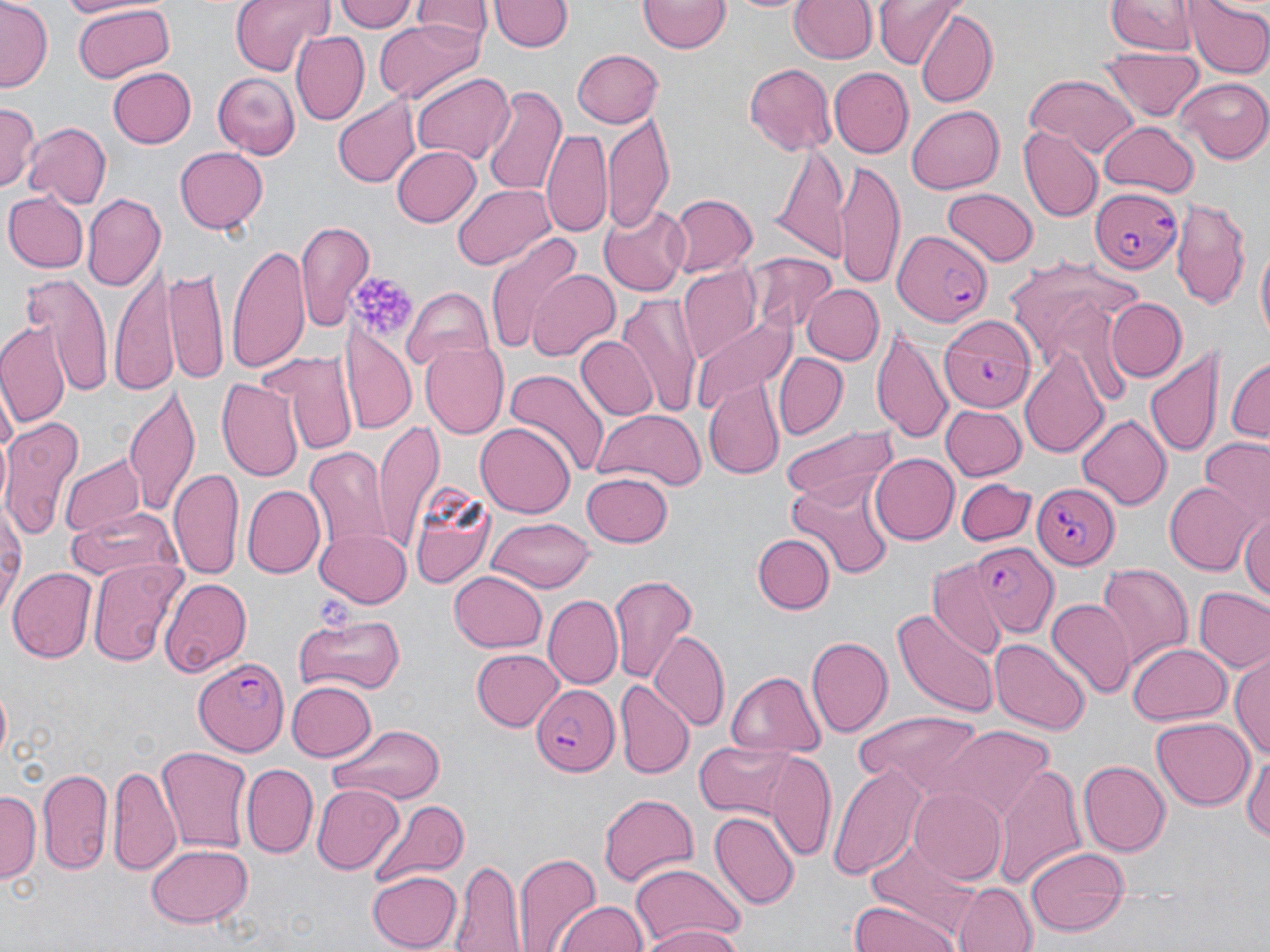
slide-level diagnosis = Plasmodium falciparum
modality = light microscopy
preparation = thin blood smear
stain = May-Grünwald-Giemsa
field of view = one of a larger specimen
image size = 1270×952 pixels
magnification = 1000x
platelet locations = approximate bounding boxes as named x1/y1/x2/y2 corners in pixels: (x1=350, y1=274, x2=417, y2=338)
uninfected red blood cell locations = approximate bounding boxes as named x1/y1/x2/y2 corners in pixels: (x1=1, y1=0, x2=51, y2=92), (x1=229, y1=0, x2=335, y2=75), (x1=333, y1=0, x2=416, y2=31), (x1=490, y1=0, x2=570, y2=54), (x1=722, y1=0, x2=814, y2=15), (x1=789, y1=0, x2=876, y2=64), (x1=872, y1=0, x2=963, y2=67), (x1=1105, y1=0, x2=1199, y2=56), (x1=410, y1=1, x2=490, y2=49), (x1=639, y1=1, x2=729, y2=54), (x1=1186, y1=1, x2=1269, y2=78), (x1=67, y1=3, x2=179, y2=82), (x1=913, y1=9, x2=997, y2=108), (x1=373, y1=20, x2=483, y2=103), (x1=291, y1=32, x2=368, y2=124), (x1=572, y1=47, x2=663, y2=128), (x1=1102, y1=48, x2=1203, y2=120), (x1=742, y1=62, x2=837, y2=155), (x1=105, y1=66, x2=196, y2=149), (x1=828, y1=69, x2=913, y2=158), (x1=411, y1=71, x2=512, y2=163), (x1=212, y1=72, x2=301, y2=159), (x1=1025, y1=73, x2=1140, y2=159), (x1=1177, y1=77, x2=1270, y2=163), (x1=479, y1=85, x2=565, y2=197), (x1=332, y1=95, x2=418, y2=189), (x1=0, y1=102, x2=39, y2=193), (x1=907, y1=103, x2=1003, y2=195), (x1=603, y1=110, x2=675, y2=233), (x1=24, y1=121, x2=113, y2=207), (x1=1098, y1=121, x2=1199, y2=198), (x1=1018, y1=125, x2=1100, y2=221), (x1=542, y1=130, x2=612, y2=241), (x1=768, y1=143, x2=851, y2=261), (x1=174, y1=145, x2=268, y2=236), (x1=391, y1=145, x2=480, y2=228), (x1=834, y1=162, x2=905, y2=287), (x1=452, y1=183, x2=554, y2=270), (x1=943, y1=188, x2=1040, y2=265), (x1=4, y1=191, x2=88, y2=272), (x1=82, y1=194, x2=165, y2=293), (x1=666, y1=194, x2=757, y2=278), (x1=1170, y1=199, x2=1251, y2=311), (x1=599, y1=204, x2=687, y2=298), (x1=295, y1=219, x2=372, y2=331), (x1=484, y1=232, x2=586, y2=354), (x1=225, y1=236, x2=312, y2=378), (x1=1253, y1=242, x2=1269, y2=354), (x1=749, y1=254, x2=836, y2=335), (x1=1002, y1=254, x2=1148, y2=387), (x1=109, y1=262, x2=177, y2=394), (x1=168, y1=263, x2=229, y2=390), (x1=678, y1=264, x2=760, y2=362), (x1=527, y1=268, x2=619, y2=360), (x1=21, y1=273, x2=113, y2=394), (x1=803, y1=283, x2=882, y2=365), (x1=403, y1=286, x2=494, y2=372), (x1=618, y1=292, x2=701, y2=419), (x1=1108, y1=298, x2=1185, y2=383), (x1=691, y1=311, x2=795, y2=418), (x1=342, y1=314, x2=416, y2=436), (x1=0, y1=317, x2=71, y2=433), (x1=873, y1=323, x2=955, y2=449), (x1=575, y1=336, x2=656, y2=421), (x1=421, y1=340, x2=509, y2=439), (x1=1145, y1=344, x2=1223, y2=465), (x1=1020, y1=348, x2=1110, y2=459), (x1=263, y1=350, x2=354, y2=455), (x1=774, y1=353, x2=847, y2=439), (x1=1226, y1=358, x2=1269, y2=446), (x1=503, y1=370, x2=609, y2=481), (x1=217, y1=374, x2=305, y2=482), (x1=704, y1=380, x2=782, y2=477), (x1=121, y1=383, x2=201, y2=518), (x1=939, y1=402, x2=1026, y2=481), (x1=591, y1=405, x2=706, y2=491), (x1=1075, y1=414, x2=1172, y2=509), (x1=4, y1=417, x2=83, y2=539), (x1=372, y1=417, x2=442, y2=551), (x1=476, y1=422, x2=574, y2=518), (x1=781, y1=424, x2=903, y2=508), (x1=1198, y1=441, x2=1270, y2=527), (x1=305, y1=445, x2=389, y2=553), (x1=868, y1=453, x2=958, y2=545), (x1=59, y1=454, x2=147, y2=541), (x1=170, y1=467, x2=245, y2=579), (x1=582, y1=473, x2=674, y2=548), (x1=786, y1=473, x2=894, y2=579), (x1=957, y1=477, x2=1035, y2=546), (x1=404, y1=480, x2=492, y2=592), (x1=1163, y1=481, x2=1258, y2=575), (x1=239, y1=484, x2=324, y2=579), (x1=0, y1=500, x2=25, y2=618), (x1=66, y1=507, x2=183, y2=587), (x1=1241, y1=508, x2=1270, y2=601), (x1=485, y1=517, x2=596, y2=591), (x1=314, y1=527, x2=411, y2=607), (x1=753, y1=534, x2=834, y2=614), (x1=87, y1=557, x2=184, y2=669), (x1=928, y1=560, x2=1010, y2=657), (x1=1094, y1=562, x2=1192, y2=670), (x1=10, y1=566, x2=96, y2=664), (x1=449, y1=570, x2=547, y2=652), (x1=607, y1=572, x2=698, y2=683), (x1=161, y1=577, x2=252, y2=680), (x1=1193, y1=587, x2=1270, y2=674), (x1=543, y1=595, x2=622, y2=687), (x1=1046, y1=598, x2=1134, y2=698), (x1=890, y1=606, x2=999, y2=719), (x1=291, y1=613, x2=408, y2=695), (x1=651, y1=631, x2=729, y2=730), (x1=805, y1=637, x2=892, y2=740), (x1=992, y1=638, x2=1088, y2=732), (x1=1128, y1=644, x2=1230, y2=728), (x1=471, y1=648, x2=563, y2=731), (x1=1232, y1=654, x2=1270, y2=765), (x1=725, y1=671, x2=825, y2=756), (x1=283, y1=680, x2=376, y2=764), (x1=614, y1=680, x2=693, y2=778), (x1=851, y1=709, x2=993, y2=799), (x1=1152, y1=715, x2=1254, y2=808), (x1=326, y1=722, x2=447, y2=806), (x1=935, y1=726, x2=1056, y2=824), (x1=692, y1=741, x2=806, y2=820), (x1=156, y1=744, x2=252, y2=856), (x1=1242, y1=747, x2=1270, y2=849), (x1=769, y1=751, x2=837, y2=862), (x1=1077, y1=760, x2=1168, y2=857), (x1=107, y1=762, x2=180, y2=873), (x1=829, y1=762, x2=926, y2=880), (x1=241, y1=763, x2=317, y2=857), (x1=993, y1=764, x2=1087, y2=889), (x1=38, y1=769, x2=113, y2=876), (x1=311, y1=784, x2=403, y2=874), (x1=909, y1=786, x2=1008, y2=885), (x1=2, y1=790, x2=38, y2=884), (x1=597, y1=793, x2=699, y2=891), (x1=369, y1=799, x2=469, y2=886), (x1=709, y1=810, x2=799, y2=910), (x1=145, y1=843, x2=254, y2=929), (x1=1026, y1=845, x2=1129, y2=936), (x1=513, y1=848, x2=603, y2=952), (x1=451, y1=859, x2=523, y2=951), (x1=628, y1=863, x2=746, y2=949), (x1=367, y1=870, x2=463, y2=950), (x1=957, y1=881, x2=1037, y2=952), (x1=848, y1=900, x2=960, y2=952), (x1=552, y1=901, x2=650, y2=952), (x1=641, y1=924, x2=745, y2=952)
Plasmodium falciparum-infected red blood cell locations = approximate bounding boxes as named x1/y1/x2/y2 corners in pixels: (x1=1088, y1=190, x2=1181, y2=275), (x1=892, y1=230, x2=996, y2=331), (x1=939, y1=315, x2=1037, y2=412), (x1=1035, y1=482, x2=1121, y2=571), (x1=969, y1=543, x2=1057, y2=638), (x1=195, y1=655, x2=291, y2=755), (x1=530, y1=684, x2=621, y2=776)